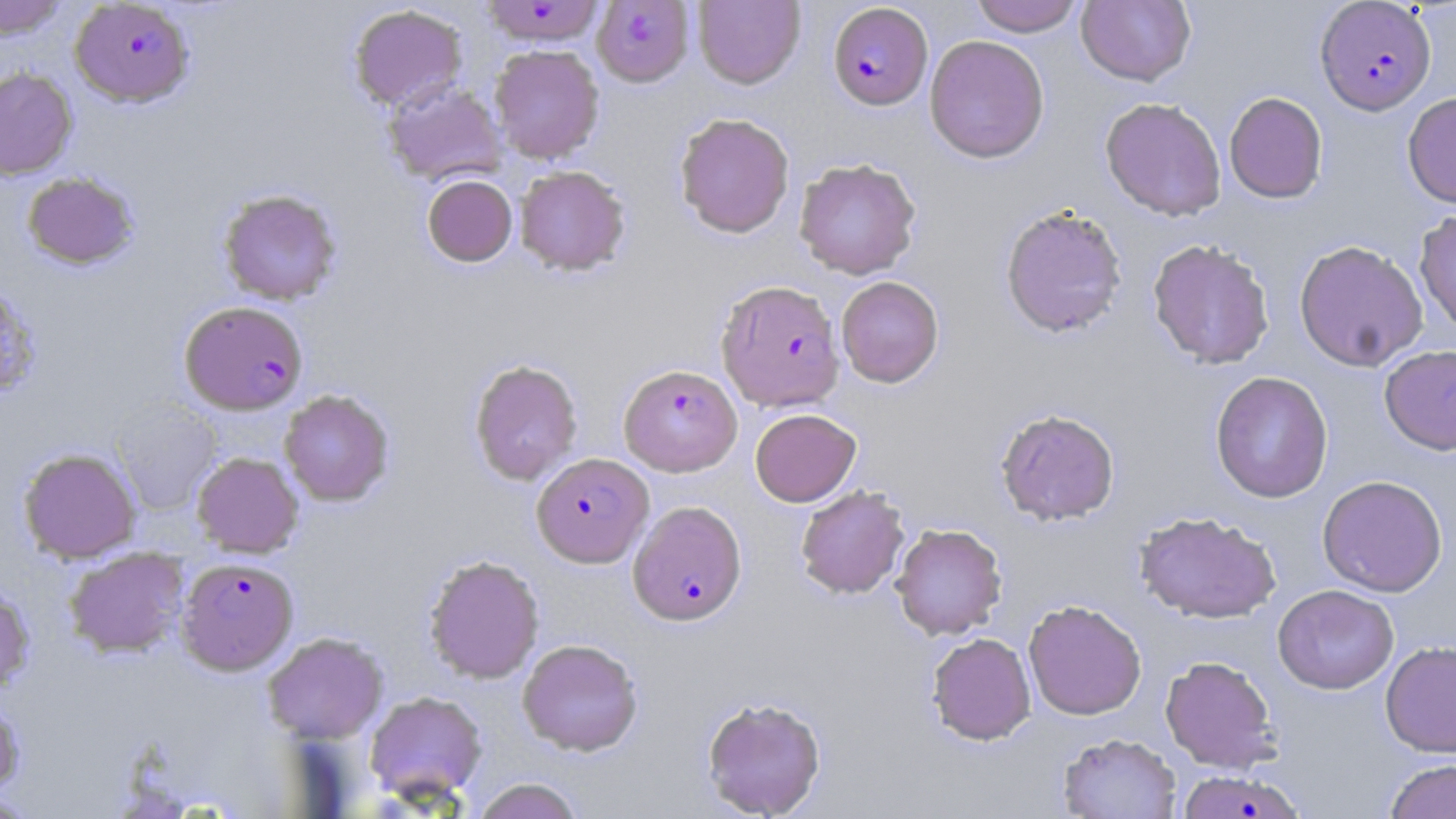
Summary:
  - Coordinate format: approximate bounding boxes as (x1, y1, x2, y2) in pixels
  - Plasmodium falciparum-infected red blood cell locations: (591, 0, 695, 87), (70, 1, 194, 107), (478, 1, 607, 47), (1315, 1, 1436, 115), (828, 3, 933, 110), (717, 280, 845, 410), (180, 300, 308, 415), (619, 364, 742, 476), (531, 453, 653, 567), (628, 500, 746, 625), (176, 557, 298, 674), (1177, 770, 1305, 818)
  - Uninfected red blood cell locations: (0, 0, 68, 40), (693, 0, 805, 89), (969, 0, 1085, 36), (1076, 0, 1196, 86), (348, 4, 468, 112), (924, 35, 1050, 163), (489, 44, 605, 164), (0, 67, 77, 180), (382, 80, 508, 186), (1224, 91, 1328, 204), (1402, 92, 1456, 208), (1100, 97, 1226, 221), (674, 112, 795, 238), (794, 158, 921, 279), (514, 165, 630, 276), (22, 171, 140, 270), (422, 174, 517, 267), (218, 189, 342, 305), (1000, 204, 1128, 339), (1414, 208, 1456, 337), (1147, 238, 1275, 369), (1294, 239, 1429, 371), (836, 276, 944, 388), (0, 285, 42, 399), (1379, 344, 1456, 456), (469, 359, 583, 485), (1210, 370, 1333, 503), (279, 390, 394, 506), (112, 402, 222, 515), (750, 408, 862, 506), (996, 408, 1120, 526), (18, 447, 141, 563), (192, 452, 304, 558), (1317, 475, 1448, 596), (796, 485, 910, 599), (1134, 511, 1281, 624), (890, 523, 1008, 640), (63, 547, 190, 658), (423, 554, 545, 684), (0, 584, 35, 694), (1272, 584, 1399, 694), (1023, 600, 1147, 720), (262, 631, 388, 744), (926, 632, 1036, 745), (517, 639, 643, 756), (1380, 640, 1456, 758), (1160, 655, 1280, 773), (364, 691, 487, 804), (701, 696, 826, 818), (0, 699, 25, 799), (1057, 733, 1181, 818), (1384, 759, 1456, 819), (472, 778, 584, 819), (0, 792, 41, 818)
  - Slide-level diagnosis: Plasmodium falciparum
  - Magnification: 1000x
  - Image size: 1456×819 pixels
  - Preparation: thin blood smear
  - Field of view: single
  - Modality: light microscopy
  - Stain: May-Grünwald-Giemsa